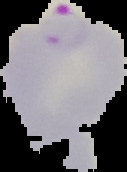
image size = 127×172 pixels
image type = cell region segmented out of the field of view; surrounding area masked to black
preparation = thin blood smear
result = malaria parasites detected